Point out Plasmodium parasites and leukocytes.
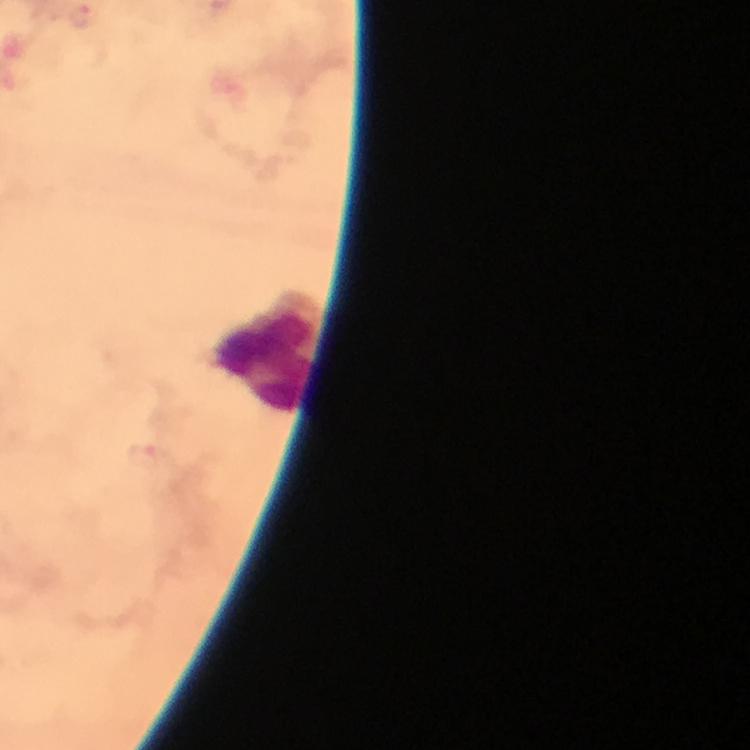

Approximate object centers, in pixels from the top-left corner.
Plasmodium parasites: (x=81, y=18), (x=146, y=456).
Leukocytes: (x=268, y=351).

Summary:
  - Capture: smartphone camera through the microscope
  - Image size: 750×750 pixels
  - Preparation: thick blood smear
  - Immersion oil: applied
  - Stain: Giemsa
  - Context: from a malaria diagnostic workup
  - Cropped from: a single field of view
  - Magnification: 100x